Identify the preparation type.
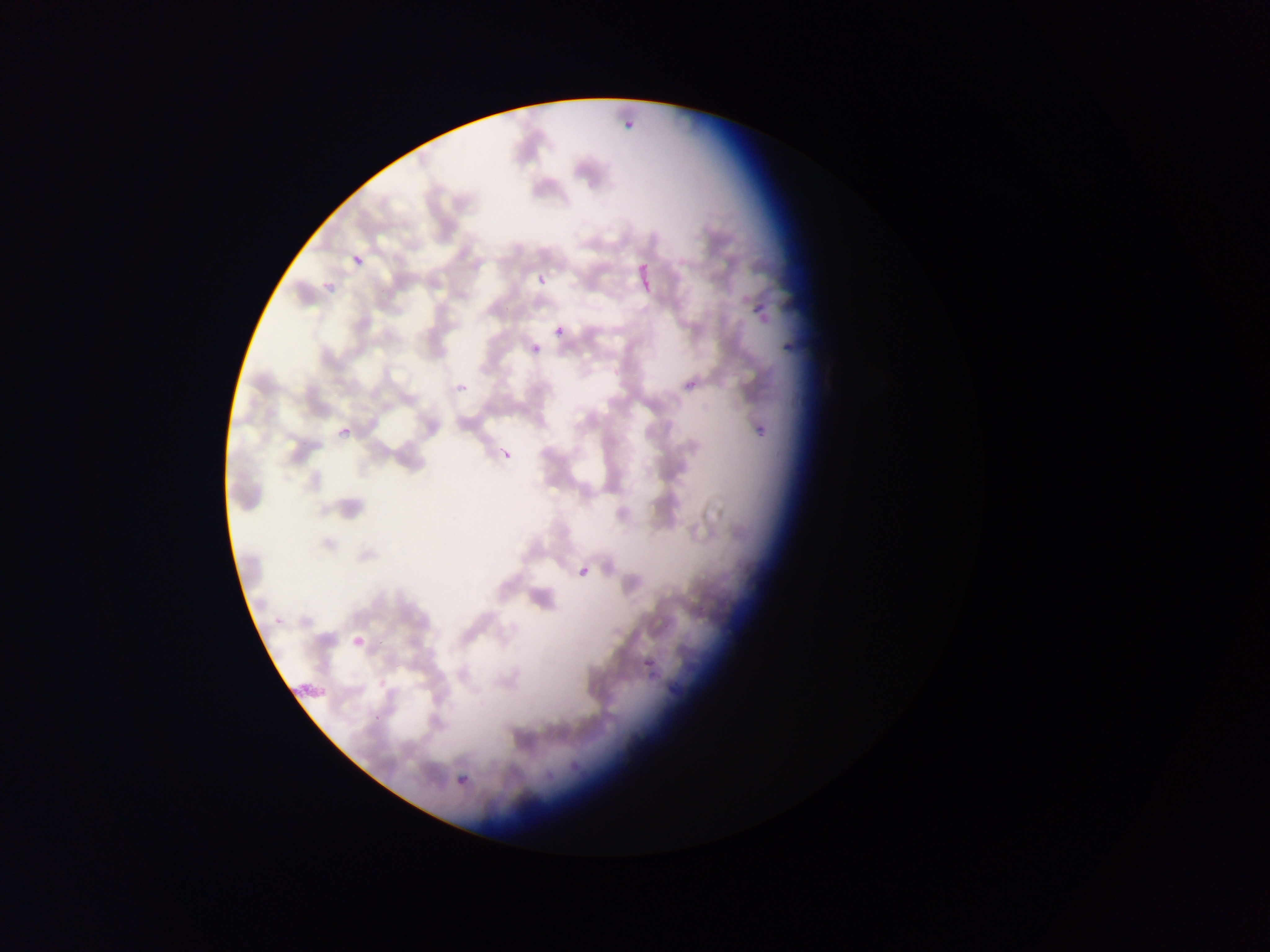
Thin blood smear.

Approximate bounding boxes as left top right bottom in pixels. Plasmodium parasite locations: 619 108 639 124; 348 251 369 266; 634 255 652 301; 531 269 559 284; 745 295 767 313; 554 325 565 336; 532 345 541 354; 457 383 468 394; 751 423 773 438; 340 427 351 438; 496 436 510 467; 572 566 592 578; 353 633 371 649; 644 649 660 669; 457 775 467 785. Sample from Ghana. One field of view. Mobile-phone photograph taken through the microscope. Image is 1270×952 pixels.